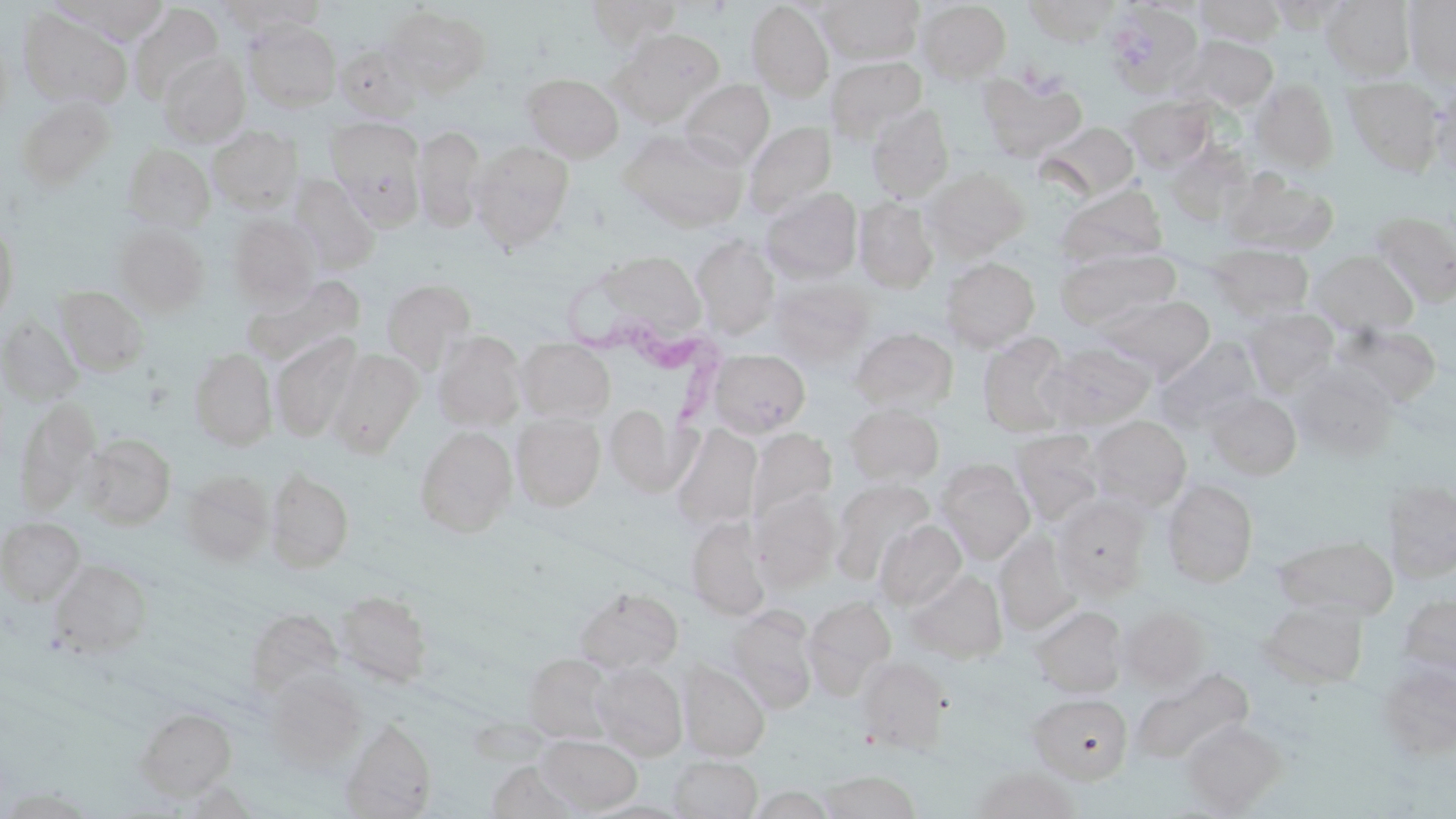
Summary:
  - Coordinate format: approximate bounding boxes as (x1, y1, x2, y2) in pixels
  - Trypanosoma brucei locations: (564, 267, 728, 419)
  - Uninfected red blood cell locations: (64, 0, 170, 43), (586, 0, 681, 48), (818, 0, 924, 64), (1023, 0, 1120, 44), (1194, 0, 1286, 46), (1266, 0, 1353, 31), (1322, 0, 1416, 81), (1404, 0, 1456, 85), (218, 1, 327, 34), (746, 1, 834, 101), (916, 1, 1011, 82), (130, 3, 223, 100), (1105, 4, 1201, 94), (385, 6, 492, 97), (18, 8, 130, 109), (246, 21, 342, 110), (609, 28, 725, 124), (0, 36, 13, 130), (1181, 36, 1278, 111), (335, 40, 426, 122), (158, 53, 250, 146), (827, 57, 927, 141), (980, 72, 1087, 160), (522, 73, 624, 162), (1343, 76, 1445, 175), (1252, 78, 1339, 173), (679, 80, 774, 168), (1430, 83, 1456, 185), (16, 95, 118, 190), (1124, 96, 1214, 172), (866, 104, 954, 201), (326, 117, 426, 224), (743, 122, 836, 219), (1040, 122, 1139, 201), (413, 125, 486, 233), (209, 126, 302, 212), (620, 129, 749, 230), (468, 141, 574, 251), (122, 144, 215, 232), (924, 167, 1028, 258), (1223, 170, 1338, 254), (288, 175, 381, 272), (1057, 185, 1168, 265), (761, 187, 862, 282), (854, 197, 938, 293), (1369, 211, 1456, 306), (228, 215, 321, 304), (0, 220, 19, 329), (113, 224, 209, 316), (692, 236, 780, 338), (1209, 244, 1314, 320), (1056, 248, 1180, 330), (586, 251, 708, 342), (1310, 251, 1419, 337), (940, 257, 1039, 351), (242, 278, 363, 365), (382, 280, 475, 372), (770, 280, 872, 366), (54, 285, 149, 376), (1104, 295, 1215, 378), (1244, 308, 1338, 395), (0, 317, 83, 405), (1336, 323, 1441, 406), (851, 327, 958, 414), (433, 331, 527, 431), (978, 333, 1074, 436), (271, 335, 361, 441), (516, 338, 615, 423), (1157, 341, 1262, 428), (1038, 343, 1156, 431), (189, 348, 277, 450), (326, 349, 422, 456), (708, 349, 810, 438), (1291, 363, 1398, 460), (1205, 391, 1302, 480), (14, 399, 101, 513), (605, 404, 691, 497), (844, 404, 945, 485), (512, 413, 606, 511), (1087, 416, 1192, 512), (670, 424, 761, 529), (414, 426, 517, 537), (748, 428, 837, 523), (1011, 429, 1107, 525), (81, 433, 176, 528), (936, 461, 1036, 562), (266, 468, 354, 571), (181, 471, 273, 564), (833, 479, 935, 578), (1162, 479, 1258, 587), (1382, 479, 1456, 581), (751, 489, 842, 590), (1052, 495, 1153, 598), (686, 516, 769, 620), (0, 517, 85, 605), (874, 519, 966, 609), (994, 532, 1081, 634), (1275, 535, 1398, 619), (47, 560, 153, 658), (906, 569, 1008, 662), (574, 586, 684, 673), (333, 590, 432, 687), (1398, 594, 1456, 676), (801, 596, 897, 694), (1261, 598, 1368, 687), (1031, 605, 1127, 697), (1118, 605, 1210, 691), (245, 609, 343, 694), (725, 609, 818, 714), (522, 653, 615, 743), (855, 656, 951, 754), (1377, 661, 1456, 760), (591, 662, 688, 760), (678, 663, 770, 761), (1130, 668, 1254, 768), (263, 672, 365, 771), (1028, 693, 1133, 783), (136, 708, 236, 797), (340, 717, 436, 818), (1180, 718, 1286, 814), (536, 734, 643, 814), (668, 755, 762, 818), (487, 760, 586, 817), (970, 767, 1082, 818), (818, 771, 921, 818), (747, 784, 837, 818)
  - Slide-level diagnosis: Trypanosoma brucei
  - Stain: May-Grünwald-Giemsa
  - Modality: optical microscopy
  - Image size: 1456×819 pixels
  - Field of view: single
  - Preparation: thin blood film
  - Magnification: 1000x